Describe the morphology of the red blood cells.
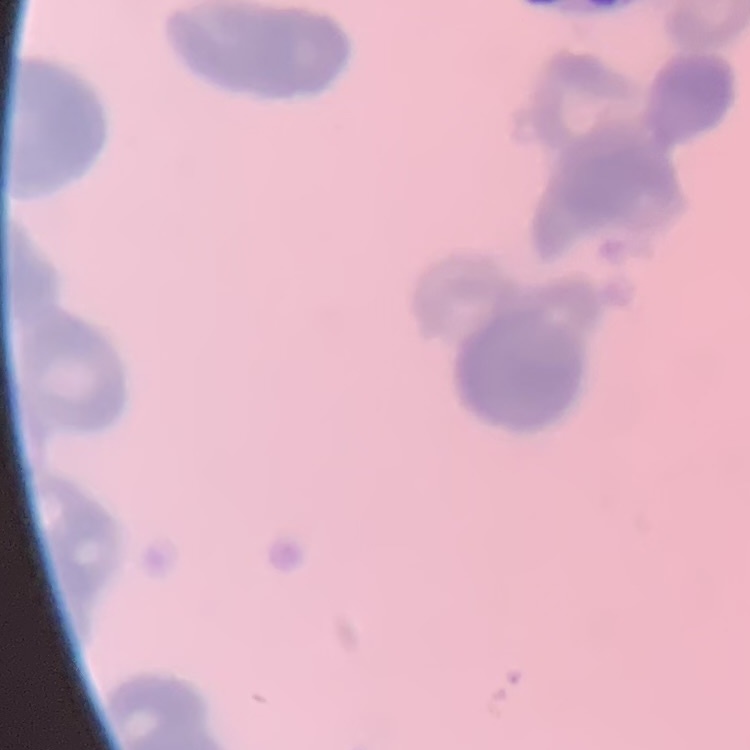

Rouleaux formation.

{
  "stain": "Field's or Giemsa",
  "preparation": "thin blood film",
  "image_type": "one tile cut from a larger photomicrograph"
}